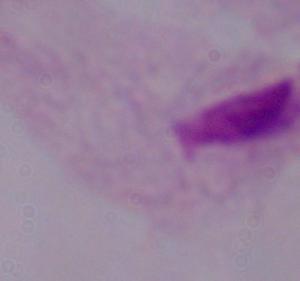

Summary:
  - Identification: trichomonad
  - Magnification: 1000x
  - Modality: photomicrograph